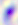 Photomicrograph. 400x magnification. Toxoplasma gondii is shown.